Assess this cell for malaria.
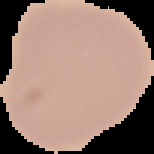

Uninfected.

preparation: thin blood smear
image_size: 154×154 pixels
image_type: segmented cell region with the area outside set to black